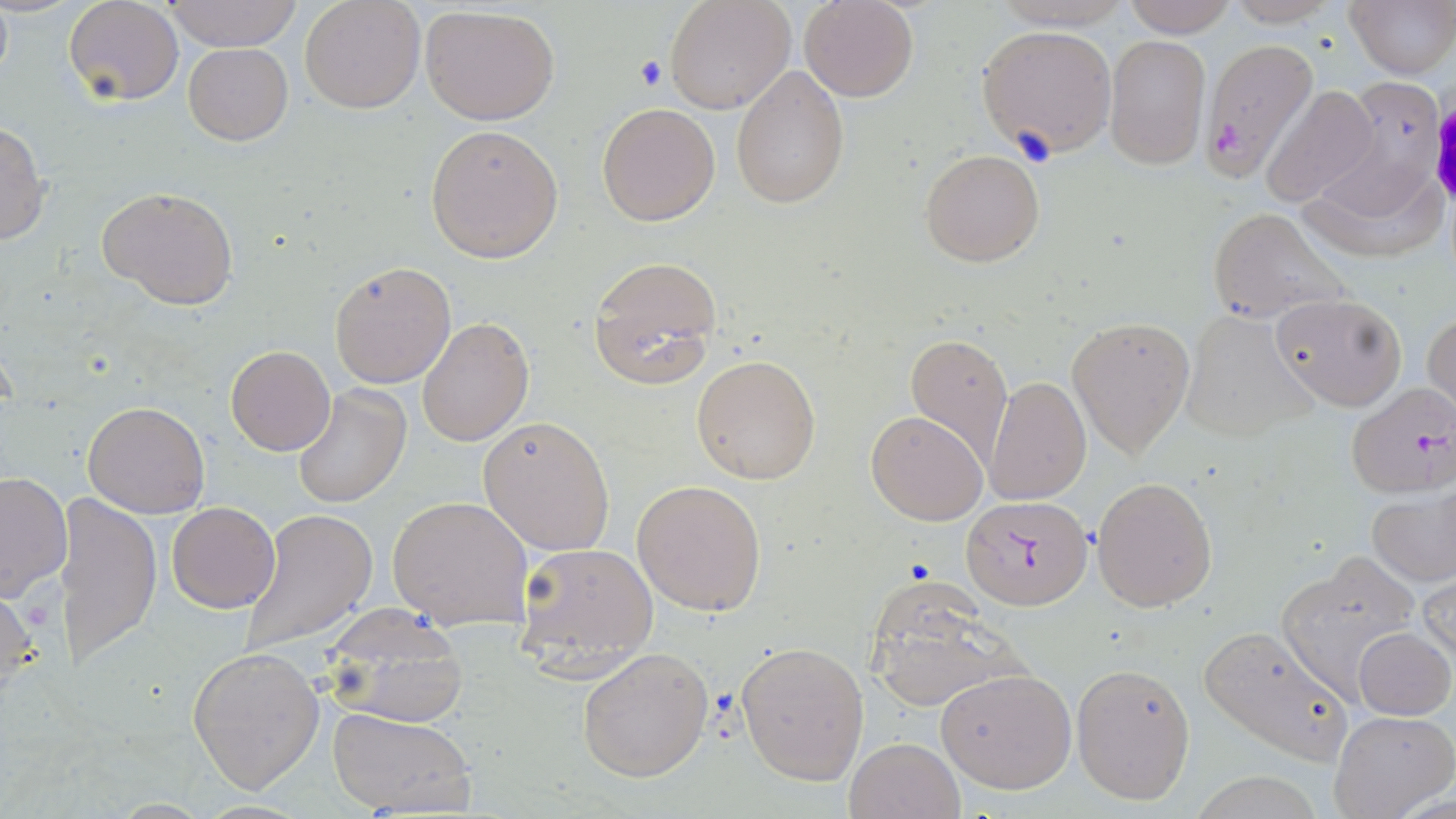
{
  "slide_level_diagnosis": "Plasmodium falciparum",
  "stain": "May-Grünwald-Giemsa",
  "field_of_view": "one of a larger specimen",
  "magnification": "1000x",
  "plasmodium_falciparum_infected_red_blood_cell_locations": "approximate bounding boxes as (x1, y1, x2, y2) in pixels: (1200, 38, 1318, 183), (1343, 384, 1456, 498), (960, 494, 1094, 610)",
  "modality": "light microscopy",
  "preparation": "thin blood film",
  "image_size": "1456×819 pixels",
  "uninfected_red_blood_cell_locations": "approximate bounding boxes as (x1, y1, x2, y2) in pixels: (166, 0, 301, 52), (299, 0, 425, 114), (666, 0, 795, 114), (799, 0, 919, 102), (982, 0, 1137, 30), (1121, 0, 1237, 38), (1344, 0, 1455, 80), (63, 1, 184, 106), (1220, 1, 1348, 26), (419, 5, 560, 125), (976, 24, 1117, 157), (1105, 35, 1212, 170), (183, 43, 293, 145), (731, 66, 850, 208), (1320, 72, 1452, 209), (1259, 84, 1381, 209), (596, 101, 722, 226), (0, 120, 49, 247), (426, 124, 564, 262), (918, 148, 1045, 267), (1296, 152, 1445, 268), (99, 186, 240, 309), (1206, 207, 1347, 323), (587, 254, 723, 389), (328, 260, 458, 389), (1270, 292, 1407, 412), (1423, 309, 1455, 425), (1179, 311, 1318, 443), (418, 316, 534, 447), (1068, 316, 1196, 459), (906, 331, 1013, 464), (225, 345, 335, 456), (691, 354, 823, 485), (985, 376, 1091, 505), (290, 383, 412, 510), (83, 401, 210, 518), (866, 410, 987, 525), (479, 416, 616, 556), (0, 471, 72, 602), (1091, 476, 1217, 611), (631, 479, 768, 616), (1365, 489, 1456, 587), (61, 494, 162, 671), (387, 494, 534, 631), (167, 501, 280, 613), (239, 508, 379, 653), (514, 541, 659, 680), (1278, 551, 1424, 697), (1223, 568, 1386, 733), (1419, 569, 1455, 669), (863, 579, 1034, 713), (0, 582, 38, 708), (319, 603, 471, 728), (1197, 625, 1355, 767), (1353, 627, 1454, 719), (736, 638, 869, 785), (187, 645, 326, 794), (575, 647, 713, 782), (1070, 661, 1195, 804), (935, 668, 1078, 793), (328, 706, 476, 816), (1328, 709, 1454, 819), (844, 737, 964, 819)"
}